Assess this cell for malaria.
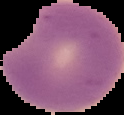

Parasitized.

image size = 124×115 pixels
preparation = thin blood smear
image type = cell region segmented out of the field of view; surrounding area masked to black